Report the malaria status of this cell.
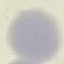
It is uninfected.

Summary:
  - Stain: Giemsa
  - Preparation: thin blood smear
  - Image type: automatically extracted cell patch, resized to 64 × 64 pixels
  - Capture: smartphone through the microscope eyepiece